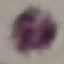

Summary:
  - Result: negative for malaria parasites
  - Stain: Giemsa
  - Capture: smartphone through the microscope eyepiece
  - Image type: automatically extracted cell patch, resized to 64 × 64 pixels
  - Preparation: thin blood smear